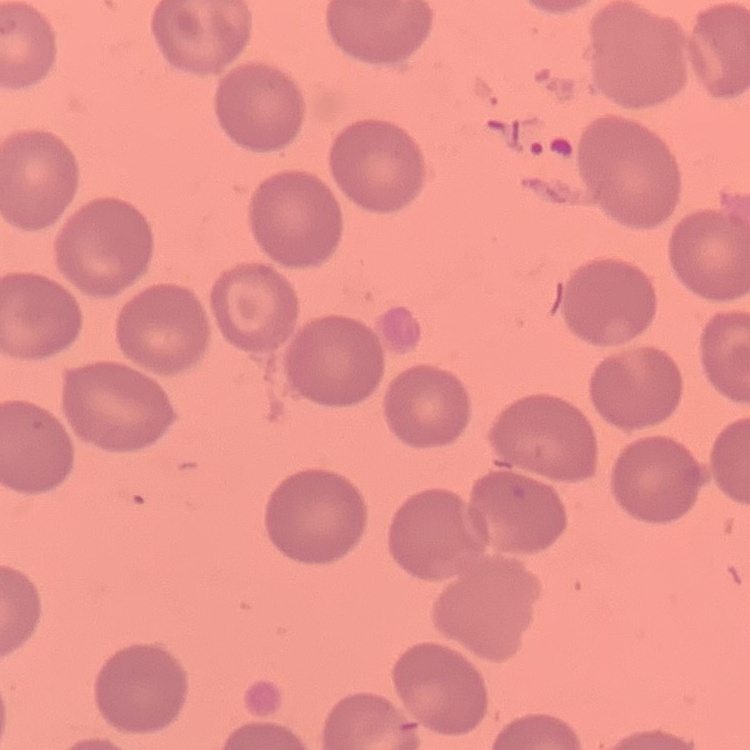
erythrocyte_morphology: no rouleaux formation
stain: Field's or Giemsa
image_type: one tile cut from a larger photomicrograph
preparation: thin blood smear